Classify this cell by malaria status.
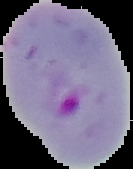

It is parasitized.

image size = 133×169 pixels
preparation = thin blood smear
image type = segmented cell region with the area outside set to black